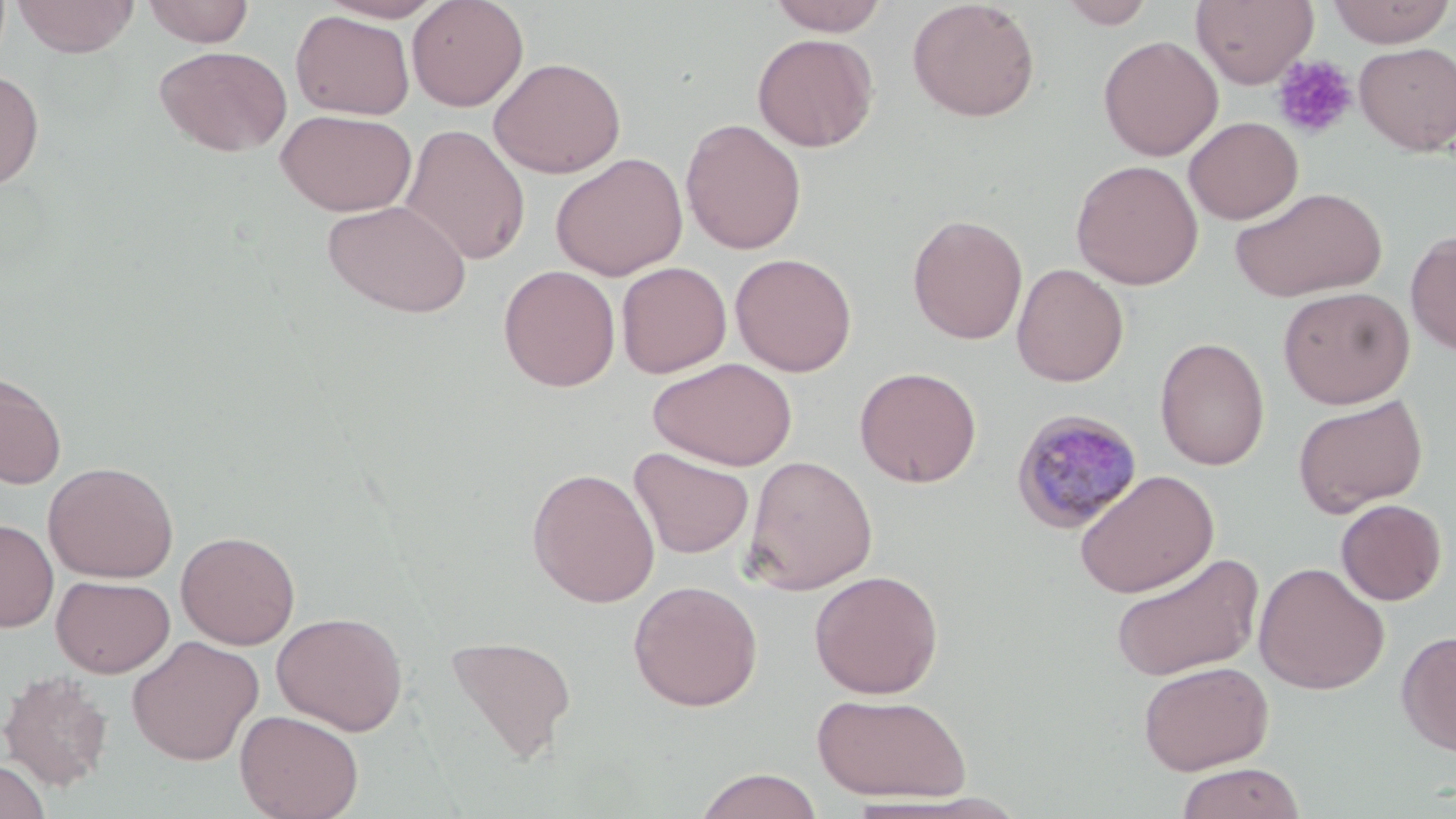

Summary:
  - Coordinate format: approximate bounding boxes as named x1/y1/x2/y2 corners in pixels
  - Platelet locations: (x1=1272, y1=55, x2=1358, y2=140)
  - Uninfected red blood cell locations: (x1=13, y1=0, x2=139, y2=57), (x1=142, y1=0, x2=254, y2=47), (x1=318, y1=0, x2=448, y2=22), (x1=407, y1=0, x2=529, y2=111), (x1=767, y1=0, x2=890, y2=36), (x1=907, y1=0, x2=1040, y2=122), (x1=1058, y1=0, x2=1156, y2=29), (x1=1191, y1=0, x2=1319, y2=89), (x1=1327, y1=0, x2=1454, y2=48), (x1=291, y1=10, x2=414, y2=120), (x1=752, y1=32, x2=878, y2=152), (x1=1098, y1=35, x2=1223, y2=161), (x1=1354, y1=42, x2=1456, y2=155), (x1=153, y1=45, x2=291, y2=157), (x1=489, y1=56, x2=626, y2=178), (x1=0, y1=68, x2=44, y2=190), (x1=276, y1=109, x2=417, y2=216), (x1=1184, y1=116, x2=1303, y2=224), (x1=680, y1=118, x2=806, y2=255), (x1=400, y1=123, x2=531, y2=266), (x1=550, y1=152, x2=688, y2=280), (x1=1071, y1=159, x2=1203, y2=290), (x1=1229, y1=186, x2=1387, y2=302), (x1=322, y1=199, x2=472, y2=318), (x1=907, y1=214, x2=1028, y2=345), (x1=1405, y1=229, x2=1456, y2=356), (x1=730, y1=252, x2=857, y2=376), (x1=616, y1=261, x2=732, y2=378), (x1=1012, y1=263, x2=1128, y2=387), (x1=498, y1=264, x2=621, y2=392), (x1=1277, y1=286, x2=1415, y2=408), (x1=1154, y1=337, x2=1270, y2=470), (x1=647, y1=357, x2=797, y2=471), (x1=854, y1=366, x2=981, y2=488), (x1=0, y1=371, x2=67, y2=490), (x1=1292, y1=395, x2=1428, y2=517), (x1=629, y1=447, x2=754, y2=559), (x1=742, y1=454, x2=878, y2=595), (x1=42, y1=461, x2=179, y2=583), (x1=527, y1=467, x2=661, y2=608), (x1=1074, y1=469, x2=1218, y2=598), (x1=1335, y1=499, x2=1447, y2=605), (x1=0, y1=518, x2=58, y2=632), (x1=176, y1=530, x2=300, y2=650), (x1=1110, y1=552, x2=1264, y2=683), (x1=1253, y1=562, x2=1390, y2=694), (x1=809, y1=570, x2=943, y2=699), (x1=52, y1=575, x2=175, y2=678), (x1=627, y1=579, x2=763, y2=712), (x1=271, y1=611, x2=408, y2=736), (x1=1396, y1=629, x2=1456, y2=757), (x1=445, y1=634, x2=577, y2=763), (x1=126, y1=635, x2=264, y2=766), (x1=1137, y1=659, x2=1274, y2=775), (x1=0, y1=670, x2=114, y2=791), (x1=811, y1=692, x2=971, y2=803), (x1=235, y1=709, x2=364, y2=819), (x1=0, y1=758, x2=52, y2=819), (x1=1175, y1=762, x2=1306, y2=819), (x1=693, y1=768, x2=824, y2=819)
  - Plasmodium malariae-infected red blood cell locations: (x1=1010, y1=409, x2=1144, y2=535)
  - Slide-level diagnosis: Plasmodium malariae
  - Field of view: single
  - Magnification: 1000x
  - Image size: 1456×819 pixels
  - Stain: May-Grünwald-Giemsa
  - Modality: light microscopy
  - Preparation: thin blood smear